State the preparation type.
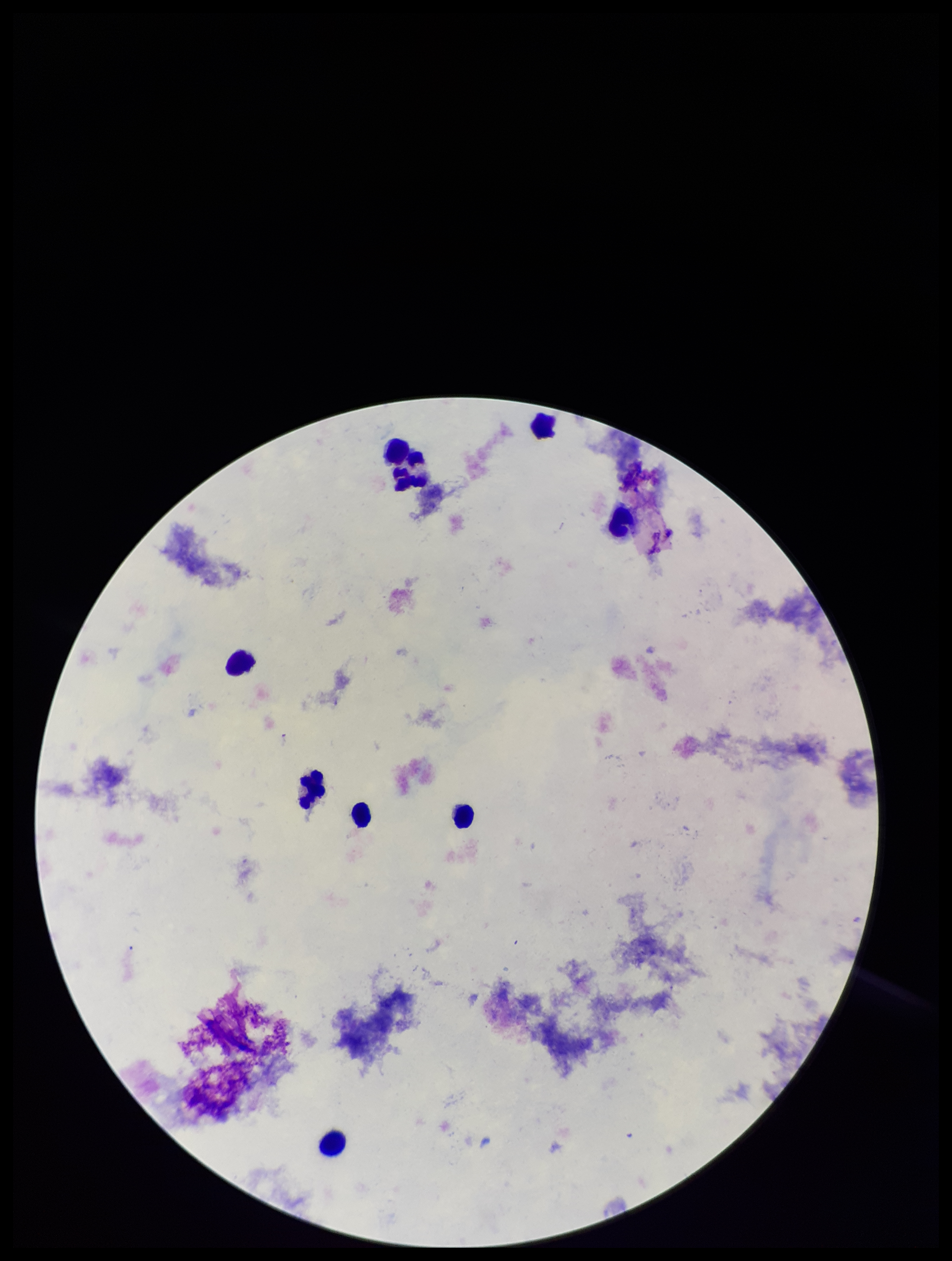

Thick.

parasite_count: 0
patient_malaria_status: negative
stain: Giemsa
image_size: 952×1261 pixels
capture: smartphone photograph through the microscope eyepiece
leukocyte_count: 9
field_of_view: single
plasmodium_parasites: none detected